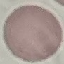

Summary:
  - Malaria status: uninfected
  - Image type: cell patch, automatically extracted from a larger field of view and resized to 64 × 64 pixels
  - Capture: smartphone through the microscope eyepiece
  - Preparation: thin blood film
  - Stain: Giemsa